Assess this cell for malaria.
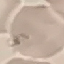

Uninfected.

Thin smear of blood. Automatically extracted cell patch, resized to 64 × 64 pixels. Photographed with a smartphone camera at the microscope eyepiece. Giemsa stain.